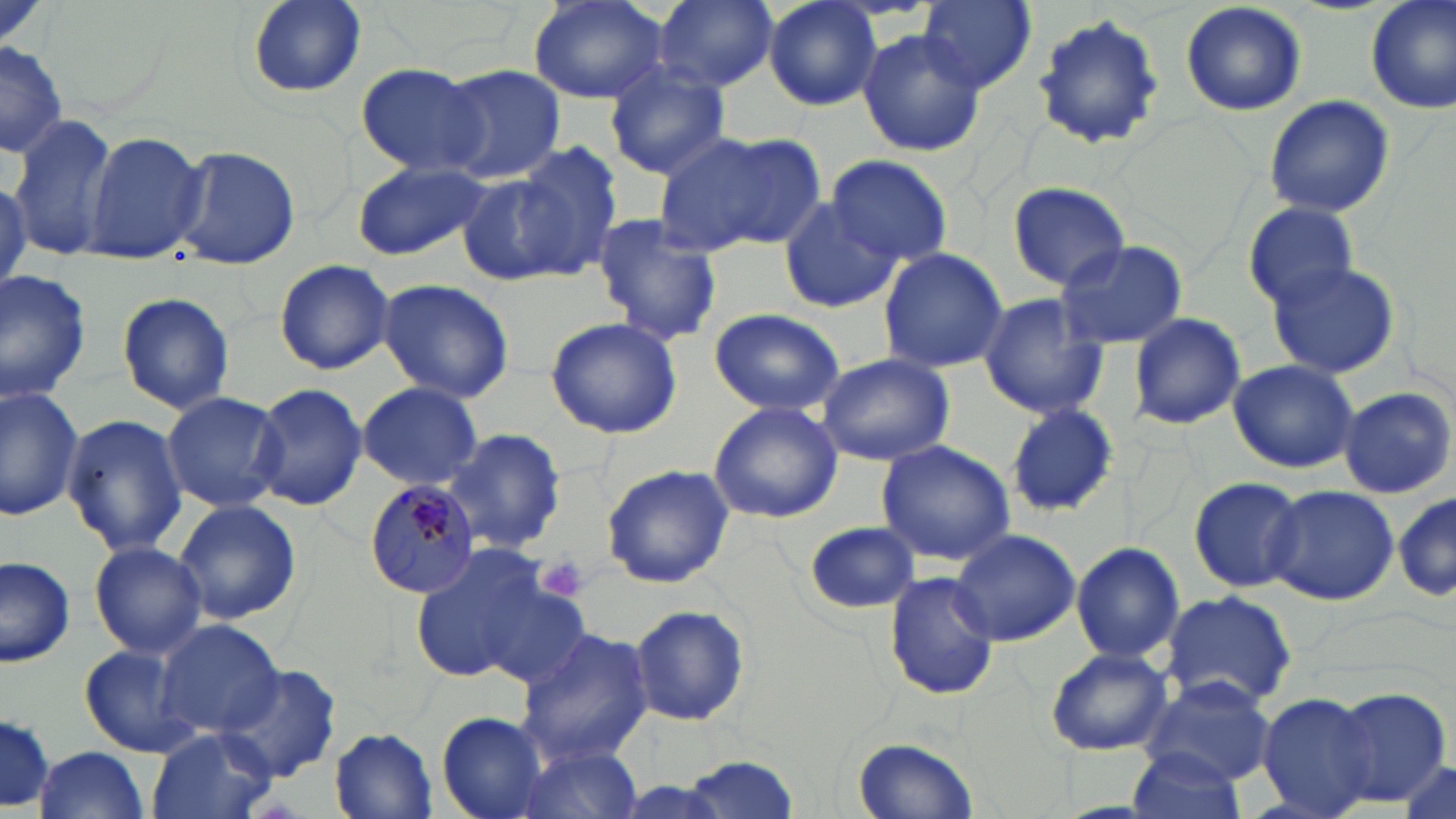
Approximate bounding boxes as named x1/y1/x2/y2 corners in pixels. Plasmodium malariae-infected red blood cell locations: (x1=362, y1=479, x2=480, y2=600). Platelet locations: (x1=537, y1=554, x2=589, y2=602). Uninfected red blood cell locations: (x1=655, y1=0, x2=778, y2=91), (x1=764, y1=0, x2=883, y2=112), (x1=918, y1=0, x2=1037, y2=92), (x1=1179, y1=0, x2=1307, y2=117), (x1=1364, y1=0, x2=1456, y2=115), (x1=243, y1=1, x2=367, y2=99), (x1=527, y1=1, x2=669, y2=105), (x1=1032, y1=11, x2=1168, y2=151), (x1=855, y1=28, x2=986, y2=158), (x1=0, y1=39, x2=68, y2=160), (x1=604, y1=62, x2=731, y2=178), (x1=355, y1=64, x2=487, y2=175), (x1=435, y1=64, x2=566, y2=184), (x1=1263, y1=95, x2=1394, y2=218), (x1=7, y1=115, x2=118, y2=259), (x1=655, y1=128, x2=824, y2=255), (x1=81, y1=130, x2=206, y2=263), (x1=511, y1=138, x2=625, y2=273), (x1=173, y1=143, x2=300, y2=271), (x1=827, y1=153, x2=954, y2=269), (x1=352, y1=159, x2=491, y2=260), (x1=456, y1=171, x2=576, y2=287), (x1=1007, y1=181, x2=1131, y2=288), (x1=777, y1=199, x2=900, y2=315), (x1=1243, y1=201, x2=1359, y2=308), (x1=589, y1=215, x2=724, y2=347), (x1=1052, y1=238, x2=1187, y2=351), (x1=877, y1=246, x2=1010, y2=373), (x1=273, y1=258, x2=396, y2=376), (x1=1265, y1=260, x2=1402, y2=380), (x1=0, y1=265, x2=91, y2=404), (x1=374, y1=278, x2=515, y2=403), (x1=116, y1=291, x2=235, y2=416), (x1=976, y1=292, x2=1109, y2=421), (x1=707, y1=307, x2=845, y2=418), (x1=1128, y1=312, x2=1246, y2=430), (x1=545, y1=314, x2=683, y2=440), (x1=817, y1=354, x2=955, y2=465), (x1=1227, y1=359, x2=1359, y2=473), (x1=251, y1=382, x2=367, y2=511), (x1=357, y1=382, x2=483, y2=490), (x1=0, y1=384, x2=85, y2=521), (x1=1339, y1=386, x2=1455, y2=498), (x1=161, y1=390, x2=287, y2=512), (x1=1003, y1=401, x2=1121, y2=516), (x1=707, y1=402, x2=843, y2=524), (x1=63, y1=414, x2=187, y2=556), (x1=442, y1=427, x2=566, y2=554), (x1=875, y1=440, x2=1016, y2=567), (x1=600, y1=463, x2=735, y2=589), (x1=1188, y1=475, x2=1307, y2=594), (x1=1266, y1=485, x2=1398, y2=607), (x1=1391, y1=489, x2=1453, y2=606), (x1=174, y1=499, x2=303, y2=625), (x1=804, y1=521, x2=919, y2=614), (x1=948, y1=527, x2=1080, y2=646), (x1=88, y1=541, x2=207, y2=657), (x1=407, y1=541, x2=562, y2=685), (x1=1071, y1=541, x2=1185, y2=664), (x1=0, y1=555, x2=74, y2=668), (x1=883, y1=571, x2=998, y2=702), (x1=473, y1=583, x2=594, y2=690), (x1=1160, y1=589, x2=1298, y2=711), (x1=628, y1=604, x2=751, y2=727), (x1=155, y1=619, x2=285, y2=738), (x1=517, y1=626, x2=656, y2=763), (x1=78, y1=643, x2=197, y2=757), (x1=1044, y1=647, x2=1173, y2=756), (x1=219, y1=664, x2=343, y2=784), (x1=1139, y1=675, x2=1278, y2=784), (x1=1329, y1=686, x2=1450, y2=808), (x1=1256, y1=691, x2=1379, y2=818), (x1=0, y1=709, x2=56, y2=812), (x1=436, y1=711, x2=552, y2=819), (x1=147, y1=726, x2=276, y2=819), (x1=330, y1=728, x2=440, y2=817), (x1=851, y1=736, x2=978, y2=819), (x1=509, y1=743, x2=645, y2=819), (x1=31, y1=745, x2=152, y2=819), (x1=1124, y1=748, x2=1248, y2=819), (x1=684, y1=753, x2=799, y2=817), (x1=1397, y1=759, x2=1453, y2=818). Slide-level diagnosis: Plasmodium malariae. Thin blood film. Light microscopy. Single field of view. Captured at 1000x magnification. May-Grünwald-Giemsa stain. Image is 1456×819 pixels.